Identify the blood parasite species.
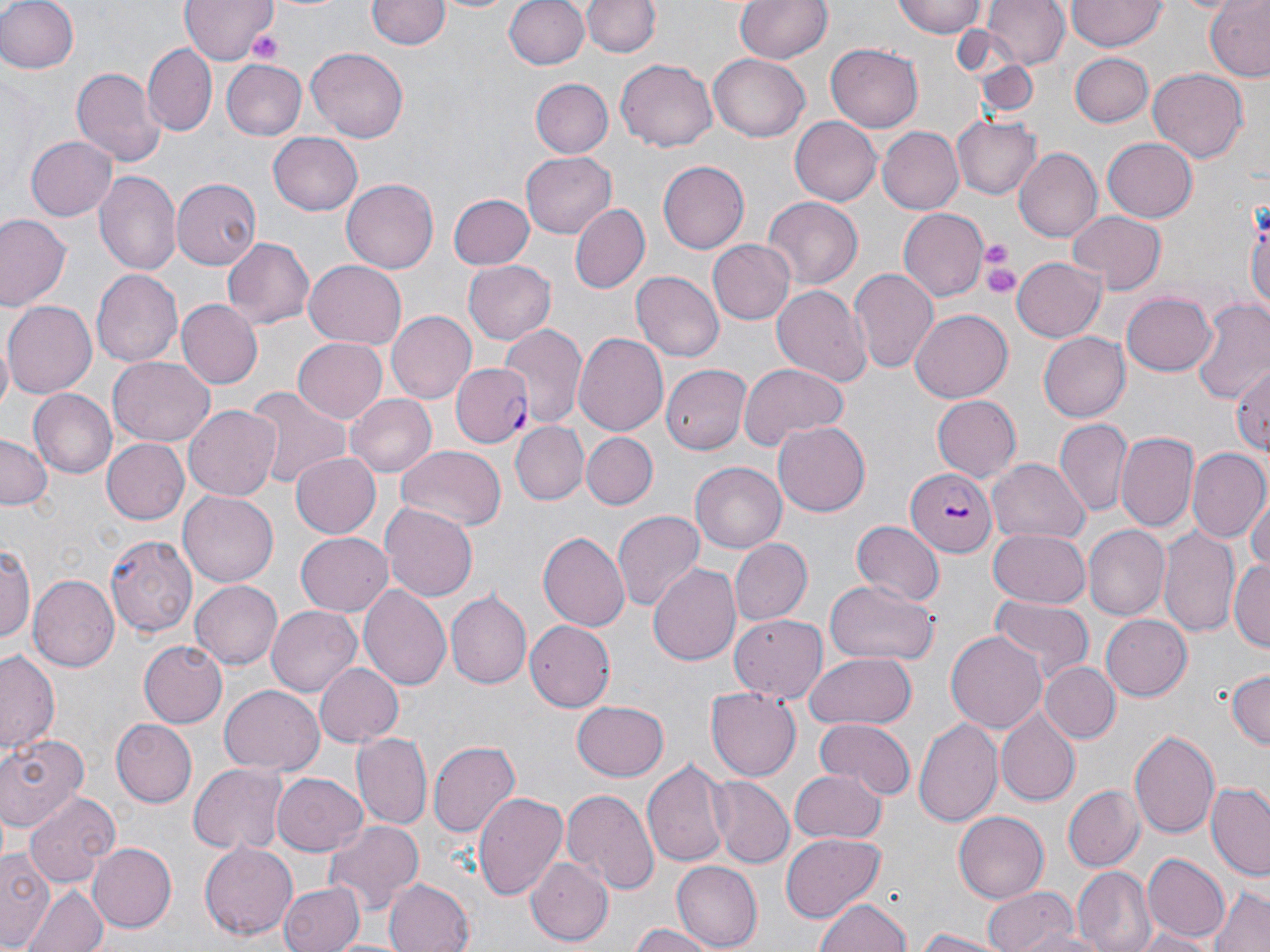

Plasmodium falciparum.

Approximate bounding boxes as [x1, y1, x2, y2] in pixels. Platelet locations: [245, 28, 285, 63], [978, 238, 1019, 283], [982, 256, 1022, 300]. Uninfected red blood cell locations: [0, 0, 78, 75], [181, 0, 277, 65], [422, 0, 524, 15], [504, 0, 589, 72], [731, 0, 834, 65], [894, 0, 988, 37], [984, 0, 1067, 69], [367, 1, 448, 53], [584, 1, 659, 58], [1066, 1, 1165, 51], [1204, 1, 1270, 82], [143, 43, 216, 134], [827, 44, 924, 131], [306, 47, 409, 141], [1068, 52, 1153, 127], [708, 54, 808, 143], [615, 58, 718, 152], [976, 58, 1036, 116], [220, 59, 306, 140], [70, 66, 165, 169], [1147, 67, 1248, 164], [531, 79, 614, 158], [952, 114, 1041, 198], [789, 117, 880, 207], [879, 126, 966, 215], [268, 132, 362, 214], [26, 135, 118, 220], [1104, 136, 1198, 221], [1014, 147, 1101, 241], [521, 151, 615, 238], [658, 161, 749, 253], [95, 169, 181, 277], [342, 176, 439, 273], [171, 177, 260, 270], [448, 194, 535, 270], [762, 196, 863, 290], [1247, 202, 1270, 325], [567, 203, 650, 295], [898, 208, 989, 301], [1065, 210, 1166, 292], [1, 215, 70, 311], [221, 237, 315, 329], [708, 239, 796, 325], [1011, 258, 1105, 344], [303, 259, 408, 347], [463, 260, 557, 346], [89, 267, 181, 367], [848, 267, 939, 375], [630, 271, 724, 362], [771, 282, 871, 384], [1120, 291, 1216, 377], [1191, 298, 1270, 400], [176, 299, 263, 388], [4, 302, 98, 398], [910, 309, 1011, 402], [387, 310, 477, 404], [500, 324, 586, 430], [1038, 331, 1130, 421], [574, 332, 668, 434], [292, 335, 387, 424], [109, 356, 215, 445], [1230, 361, 1270, 457], [737, 362, 846, 450], [660, 364, 750, 456], [244, 384, 350, 495], [27, 390, 116, 479], [346, 393, 436, 477], [931, 395, 1021, 482], [184, 405, 279, 500], [1055, 420, 1133, 518], [772, 421, 870, 516], [511, 422, 588, 504], [1117, 431, 1198, 534], [582, 432, 657, 510], [0, 434, 49, 513], [102, 440, 189, 523], [395, 446, 507, 532], [1187, 450, 1269, 545], [290, 452, 379, 538], [988, 458, 1090, 545], [689, 461, 787, 554], [178, 491, 278, 587], [1248, 495, 1270, 577], [378, 504, 478, 599], [611, 508, 705, 612], [852, 519, 942, 605], [1084, 526, 1170, 620], [988, 527, 1090, 608], [1159, 528, 1241, 641], [537, 530, 629, 633], [296, 533, 392, 616], [104, 534, 197, 637], [728, 538, 811, 625], [0, 539, 35, 648], [1228, 557, 1270, 651], [647, 563, 742, 668], [27, 574, 118, 672], [192, 579, 284, 669], [824, 579, 938, 666], [358, 583, 451, 691], [446, 591, 530, 689], [986, 598, 1094, 691], [266, 606, 361, 697], [1102, 613, 1192, 702], [731, 615, 829, 703], [525, 622, 615, 710], [946, 630, 1047, 734], [137, 639, 227, 728], [0, 648, 62, 761], [804, 652, 916, 729], [313, 663, 403, 747], [1043, 663, 1118, 742], [1225, 668, 1269, 752], [219, 685, 324, 775], [706, 686, 801, 780], [570, 701, 669, 781], [996, 710, 1081, 809], [914, 714, 1004, 831], [814, 716, 915, 800], [109, 719, 195, 807], [0, 730, 90, 833], [1130, 730, 1219, 839], [350, 734, 430, 830], [427, 737, 521, 843], [642, 757, 731, 868], [188, 763, 287, 854], [790, 769, 884, 846], [271, 771, 368, 857], [711, 777, 793, 869], [1206, 780, 1270, 879], [1063, 784, 1146, 871], [561, 788, 658, 896], [472, 790, 568, 902], [24, 792, 121, 887], [953, 811, 1050, 904], [323, 820, 424, 916], [779, 832, 884, 923], [199, 841, 297, 941], [88, 842, 176, 933], [1, 848, 51, 950], [1141, 852, 1230, 942], [527, 855, 613, 943], [671, 862, 764, 949], [1073, 866, 1154, 952], [383, 877, 476, 952], [277, 880, 364, 952], [982, 884, 1080, 952], [25, 886, 107, 952], [1207, 886, 1270, 952], [815, 897, 913, 952], [626, 922, 718, 952], [1013, 924, 1109, 952], [1126, 924, 1218, 952], [912, 927, 1016, 951]. Plasmodium falciparum-infected red blood cell locations: [453, 363, 534, 449], [905, 465, 995, 556]. Light microscopy. Image is 1270×952 pixels. Thin blood film. May-Grünwald-Giemsa stain. Captured at 1000x magnification. One field of a larger specimen.